Give the position of every Plasmodium parasite visible.
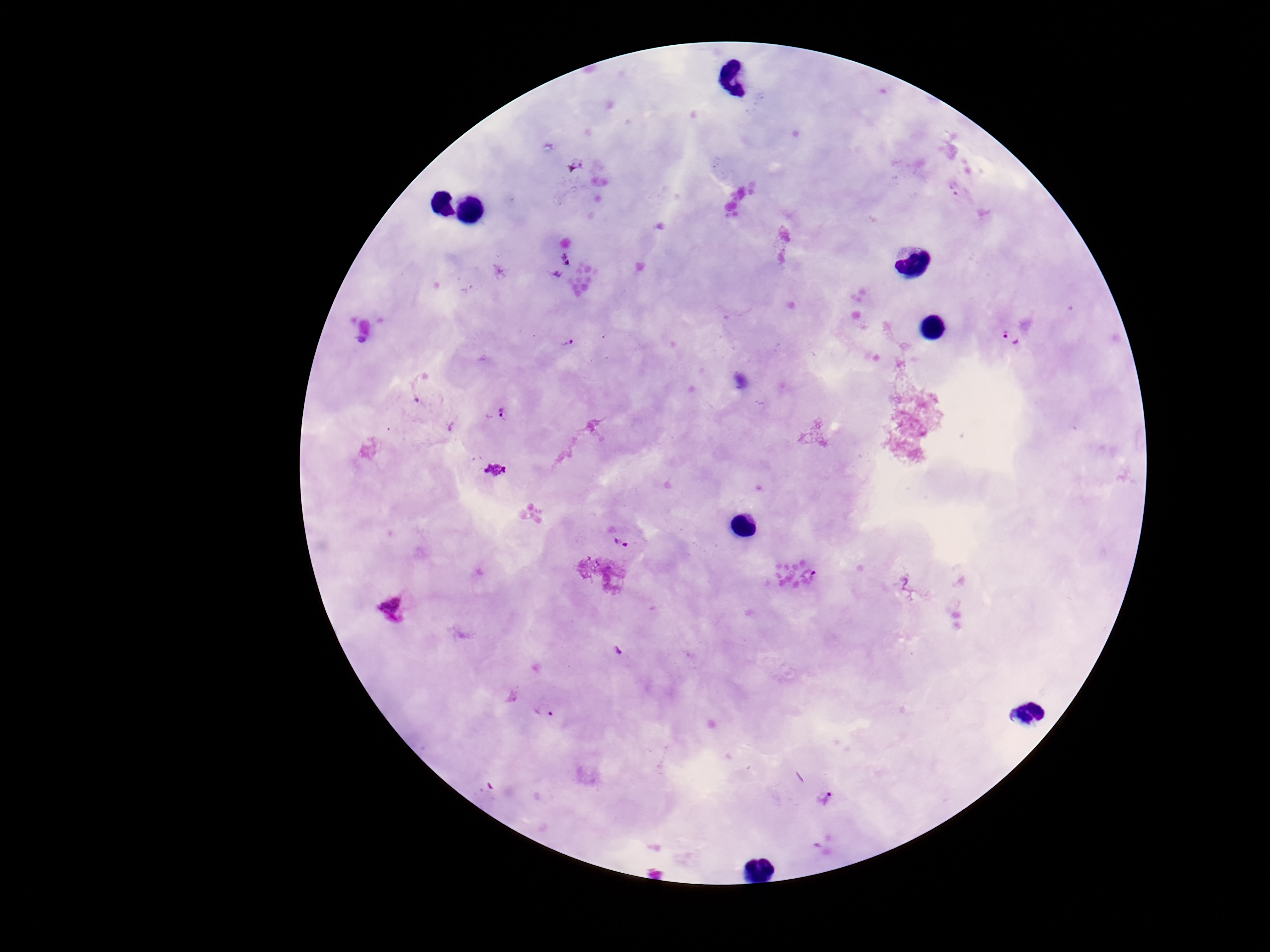

Approximate object centers, in pixels from the top-left corner.
Plasmodium parasites: (x=1012, y=338), (x=567, y=343), (x=501, y=413), (x=621, y=545), (x=617, y=651), (x=543, y=711), (x=824, y=798).

preparation = thick blood film
patient malaria status = positive
image size = 1270×952 pixels
field of view = one from this slide
magnification = 100x
stain = Giemsa
capture = smartphone camera through the microscope eyepiece